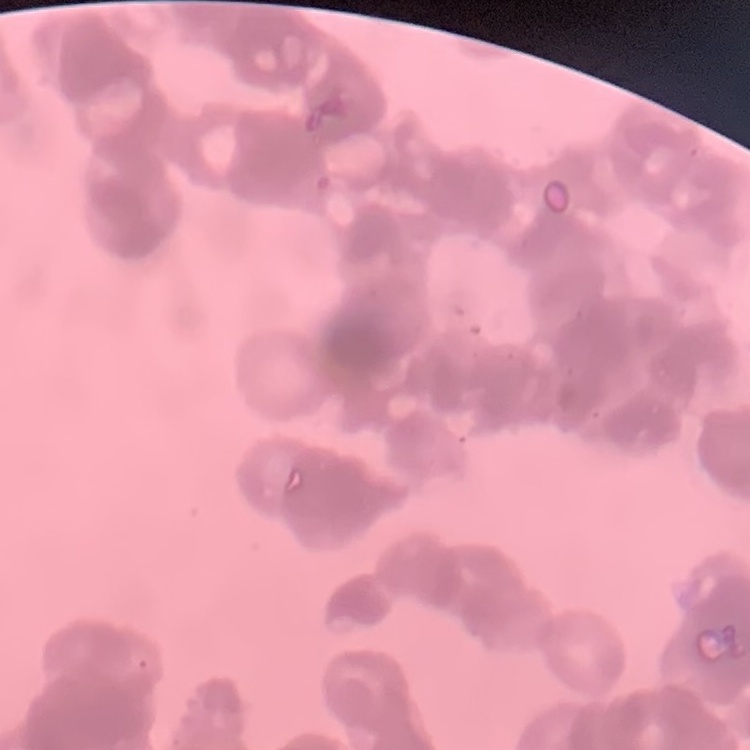
red blood cell morphology = rouleaux formation
image type = one tile cut from a larger photomicrograph
stain = Field's or Giemsa
preparation = thin blood smear